Outline each blood parasite and name the species.
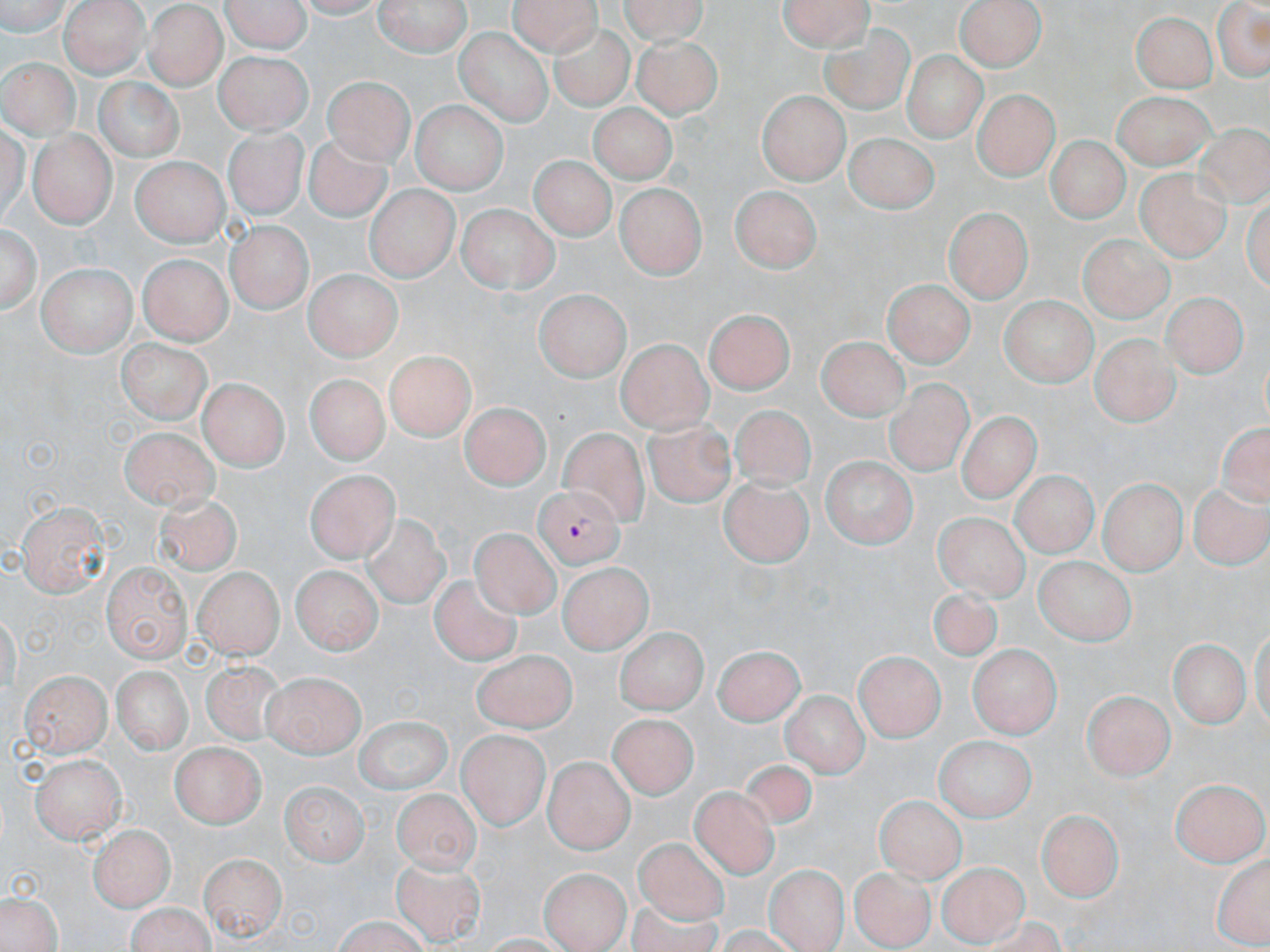

Approximate bounding boxes as (x1, y1, x2, y2) in pixels.
Plasmodium falciparum-infected red blood cells: (533, 482, 622, 565).
No Plasmodium ovale, Plasmodium malariae, Plasmodium vivax, Babesia divergens, or Trypanosoma brucei observed.

{
  "slide_level_diagnosis": "Plasmodium falciparum",
  "uninfected_red_blood_cell_locations": "approximate bounding boxes as (x1, y1, x2, y2) in pixels: (0, 0, 76, 35), (59, 0, 146, 77), (220, 0, 311, 52), (372, 0, 470, 55), (508, 0, 603, 52), (618, 0, 715, 42), (775, 0, 878, 50), (1210, 0, 1269, 85), (958, 1, 1044, 72), (142, 6, 224, 89), (1131, 8, 1218, 91), (552, 24, 634, 107), (456, 28, 554, 127), (820, 29, 913, 111), (635, 34, 720, 117), (215, 50, 309, 133), (901, 50, 986, 139), (0, 57, 79, 136), (324, 73, 414, 164), (95, 76, 183, 161), (972, 88, 1058, 181), (758, 89, 846, 183), (1110, 90, 1213, 166), (590, 100, 674, 186), (414, 103, 506, 193), (1193, 122, 1270, 212), (226, 128, 305, 218), (306, 130, 391, 226), (26, 131, 113, 226), (841, 132, 938, 214), (1044, 137, 1126, 225), (532, 154, 616, 238), (133, 155, 227, 247), (1136, 167, 1231, 262), (616, 184, 705, 281), (732, 184, 820, 274), (366, 186, 456, 280), (458, 201, 560, 290), (944, 205, 1033, 301), (2, 220, 39, 316), (229, 223, 309, 312), (1081, 231, 1173, 319), (138, 252, 232, 346), (37, 259, 136, 355), (303, 269, 399, 362), (884, 278, 973, 368), (533, 290, 627, 383), (1161, 291, 1246, 378), (999, 294, 1103, 384), (706, 306, 794, 391), (1091, 331, 1177, 427), (115, 334, 216, 425), (817, 335, 907, 421), (619, 339, 710, 431), (384, 348, 476, 440), (305, 372, 389, 457), (199, 377, 287, 471), (887, 378, 975, 480), (460, 404, 557, 488), (730, 404, 815, 488), (643, 409, 739, 512), (953, 410, 1043, 509), (120, 423, 218, 511), (558, 425, 650, 523), (822, 456, 915, 549), (305, 469, 396, 561), (1009, 470, 1093, 558), (718, 476, 814, 566), (1098, 478, 1185, 574), (1187, 480, 1267, 570), (155, 490, 245, 576), (16, 497, 115, 597), (930, 511, 1034, 606), (359, 515, 456, 612), (471, 524, 559, 615), (1031, 557, 1133, 647), (104, 561, 192, 662), (558, 561, 648, 653), (294, 563, 380, 656), (196, 567, 282, 656), (428, 574, 525, 670), (918, 587, 1007, 663), (616, 624, 702, 711), (1166, 642, 1250, 731), (970, 643, 1062, 735), (711, 644, 805, 724), (856, 649, 942, 741), (474, 650, 580, 732), (199, 659, 291, 743), (111, 664, 192, 758), (19, 668, 112, 756), (261, 670, 364, 756), (1085, 687, 1175, 779), (778, 690, 872, 779), (614, 709, 697, 796), (355, 719, 453, 796), (457, 731, 549, 828), (930, 736, 1038, 824), (171, 741, 266, 827), (35, 751, 128, 842), (736, 756, 819, 832), (546, 757, 632, 850), (1173, 775, 1266, 867), (280, 778, 368, 865), (684, 783, 783, 879), (390, 785, 477, 872), (873, 797, 965, 892), (1032, 806, 1123, 903), (88, 825, 174, 911), (632, 835, 735, 930), (201, 848, 287, 939), (1211, 853, 1270, 949), (392, 858, 484, 943), (938, 863, 1029, 947), (767, 865, 846, 950), (850, 866, 936, 948), (539, 867, 629, 952), (1, 887, 64, 952), (123, 899, 219, 952), (324, 916, 435, 950)",
  "magnification": "1000x",
  "image_size": "1270×952 pixels",
  "preparation": "thin blood smear",
  "stain": "May-Grünwald-Giemsa",
  "modality": "light microscopy",
  "field_of_view": "one of a larger specimen"
}